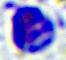

Summary:
  - Identification: leukocyte
  - Modality: photomicrograph
  - Magnification: 400x